Locate and identify every blood parasite.
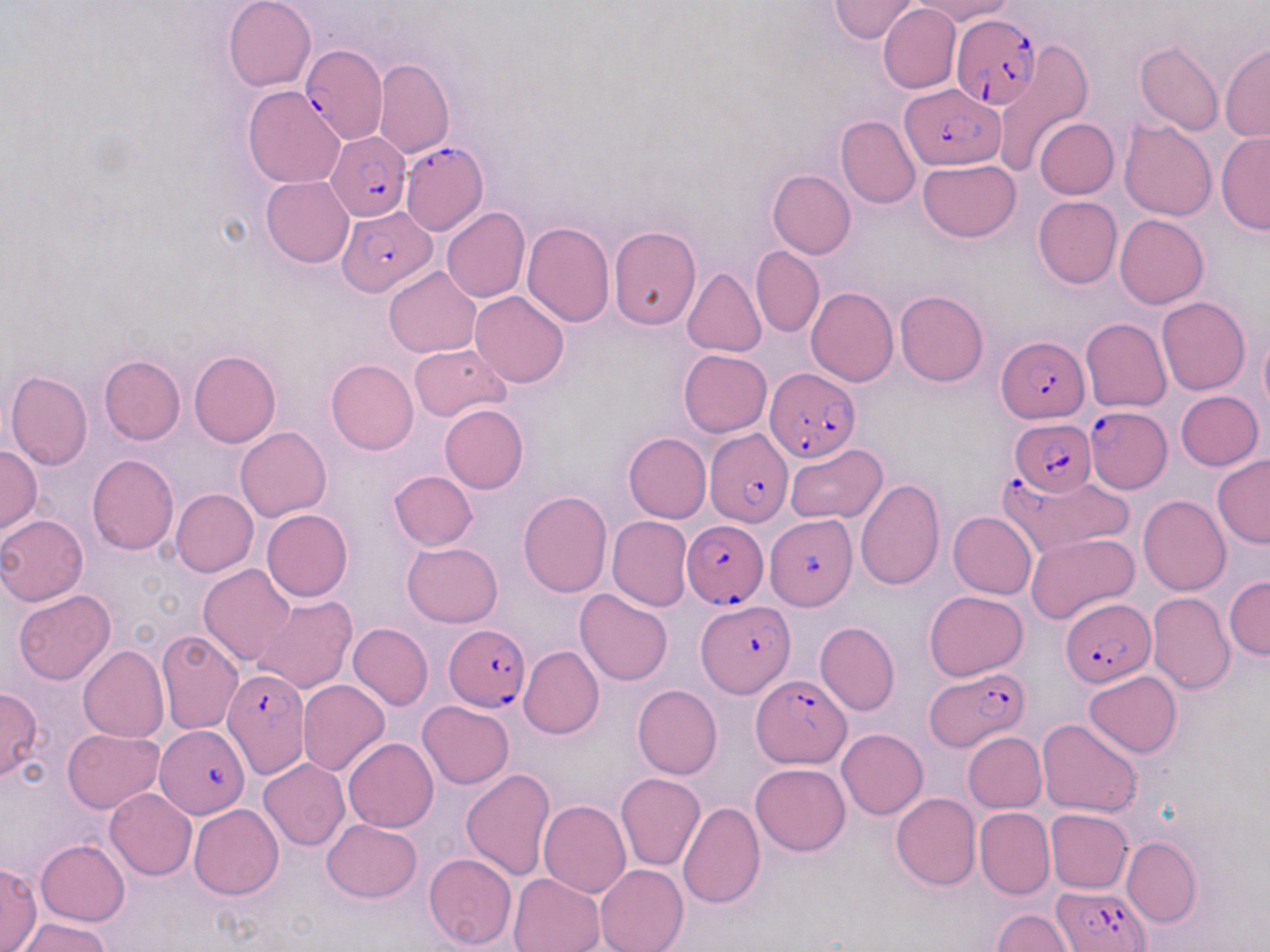

Approximate bounding boxes as (x1, y1, x2, y2) in pixels.
Plasmodium falciparum-infected red blood cells: (951, 13, 1041, 109), (299, 44, 385, 144), (901, 83, 1006, 171), (327, 131, 411, 221), (400, 140, 487, 236), (337, 206, 438, 296), (998, 336, 1087, 422), (765, 367, 858, 463), (1085, 406, 1173, 494), (1009, 418, 1097, 496), (704, 427, 793, 527), (1000, 472, 1134, 558), (767, 511, 855, 607), (682, 520, 769, 607), (1060, 597, 1156, 685), (696, 598, 794, 698), (444, 623, 530, 712), (923, 666, 1029, 750), (221, 668, 308, 780), (752, 674, 850, 768), (156, 725, 250, 818), (1055, 886, 1148, 952).
No Plasmodium ovale, Plasmodium malariae, Plasmodium vivax, Babesia divergens, or Trypanosoma brucei observed.

Summary:
  - Uninfected red blood cell locations: (224, 0, 317, 91), (829, 0, 918, 43), (915, 0, 1014, 25), (878, 4, 960, 95), (992, 39, 1092, 175), (1134, 41, 1224, 136), (1220, 45, 1270, 143), (372, 58, 454, 160), (242, 85, 345, 188), (835, 115, 920, 210), (1034, 118, 1119, 199), (1119, 119, 1218, 221), (1217, 130, 1270, 234), (917, 159, 1021, 242), (767, 170, 856, 259), (260, 176, 353, 268), (1033, 196, 1122, 289), (441, 207, 530, 304), (1115, 214, 1209, 309), (521, 221, 614, 326), (609, 227, 701, 329), (751, 245, 824, 337), (385, 266, 481, 358), (682, 268, 766, 358), (806, 287, 898, 387), (470, 290, 569, 388), (895, 290, 988, 386), (1156, 297, 1250, 395), (1081, 318, 1171, 412), (1259, 328, 1270, 417), (410, 342, 512, 420), (189, 349, 281, 448), (678, 349, 773, 437), (98, 355, 186, 445), (325, 360, 418, 454), (6, 371, 93, 471), (1176, 391, 1263, 471), (439, 404, 528, 494), (235, 426, 332, 521), (623, 433, 711, 523), (784, 442, 887, 524), (0, 444, 41, 533), (87, 453, 179, 555), (1212, 455, 1270, 549), (387, 471, 477, 552), (855, 479, 945, 590), (171, 489, 258, 576), (518, 491, 613, 597), (1138, 494, 1230, 595), (261, 508, 352, 602), (948, 511, 1036, 599), (0, 514, 88, 605), (608, 516, 693, 611), (1027, 531, 1140, 625), (402, 542, 503, 626), (199, 564, 295, 666), (1224, 576, 1270, 659), (13, 590, 115, 685), (574, 590, 673, 687), (925, 590, 1028, 680), (1147, 592, 1235, 693), (251, 594, 358, 695), (815, 620, 899, 716), (348, 623, 433, 710), (155, 628, 243, 733), (79, 646, 169, 742), (518, 646, 604, 739), (1083, 669, 1181, 758), (298, 680, 390, 776), (633, 685, 722, 780), (0, 688, 43, 781), (417, 700, 513, 788), (1037, 718, 1142, 817), (62, 728, 165, 812), (836, 728, 928, 820), (963, 732, 1046, 812), (344, 738, 438, 832), (259, 758, 350, 850), (750, 763, 850, 856), (460, 769, 556, 880), (616, 772, 705, 871), (105, 788, 197, 880), (891, 793, 981, 890), (538, 801, 631, 899), (677, 801, 764, 907), (188, 804, 284, 899), (974, 807, 1054, 899), (1045, 809, 1133, 892), (324, 819, 422, 901), (1122, 837, 1201, 927), (35, 840, 130, 926), (424, 853, 519, 949), (0, 863, 41, 952), (597, 864, 687, 952), (508, 873, 605, 952), (993, 909, 1073, 951), (16, 917, 112, 952)
  - Slide-level diagnosis: Plasmodium falciparum
  - Preparation: thin blood smear
  - Image size: 1270×952 pixels
  - Stain: May-Grünwald-Giemsa
  - Field of view: one of a larger specimen
  - Modality: light microscopy
  - Magnification: 1000x